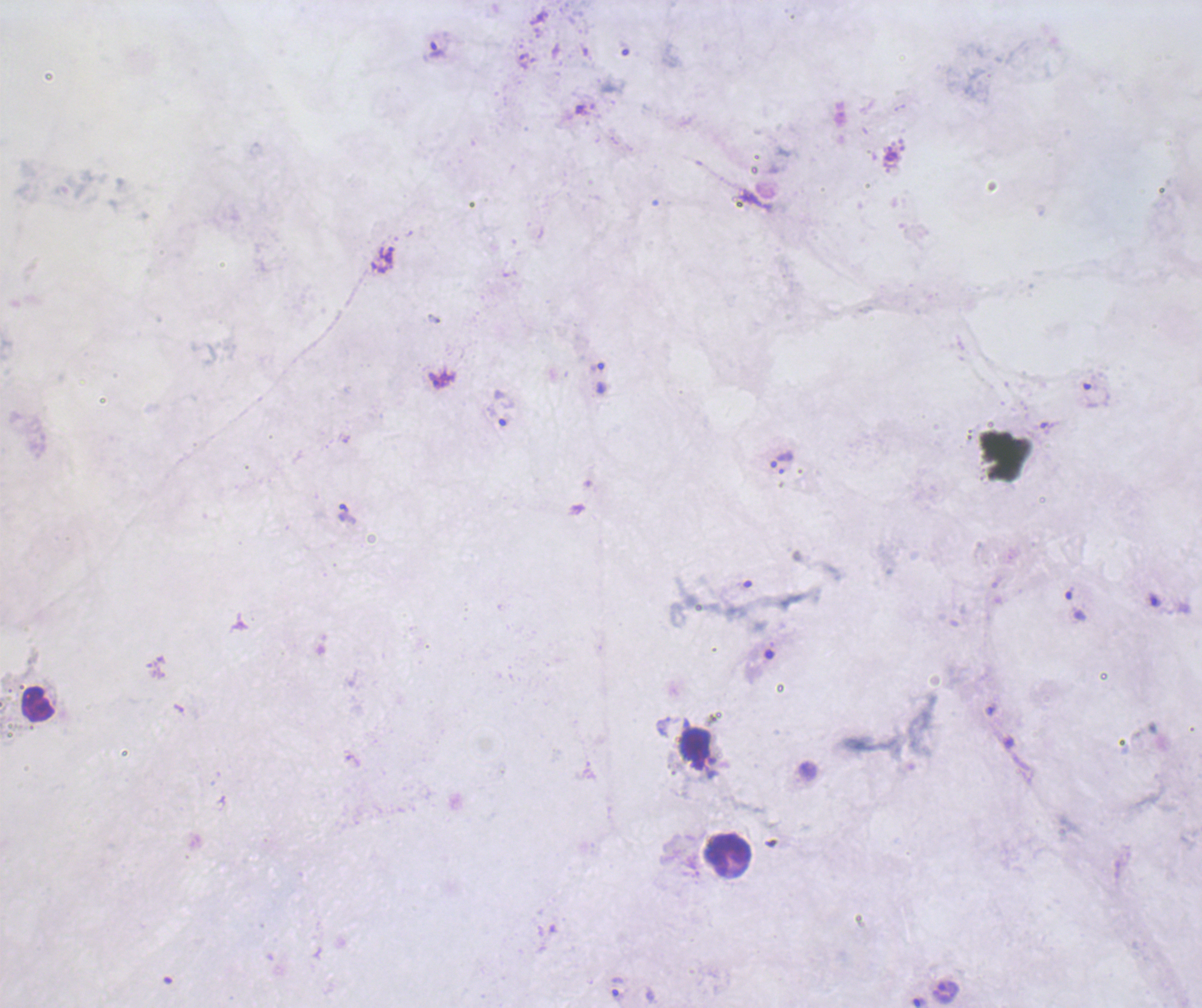
Approximate centers as (x, y) in pixels.
Summary:
  - Leukocyte locations: (37, 704), (694, 748), (728, 853)
  - Trophozoite locations: (437, 50), (601, 378), (442, 381), (1096, 395), (501, 408), (782, 459), (346, 513), (1075, 604), (619, 988), (945, 993)
  - Coloration quality: bad
  - Magnification: 100x
  - Field of view: one from this slide
  - Stain: Romanowsky
  - Preparation: thick smear of blood
  - Background quality: unsatisfactory
  - Result: Plasmodium parasites identified
  - Image size: 1202×1008 pixels
  - Context: previously used in a real diagnosis